Classify this cell by malaria status.
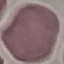

Uninfected.

capture = smartphone camera at the microscope eyepiece
image type = automatically extracted cell patch, resized to 64 × 64 pixels
preparation = thin blood smear
stain = Giemsa